State the blood parasite species.
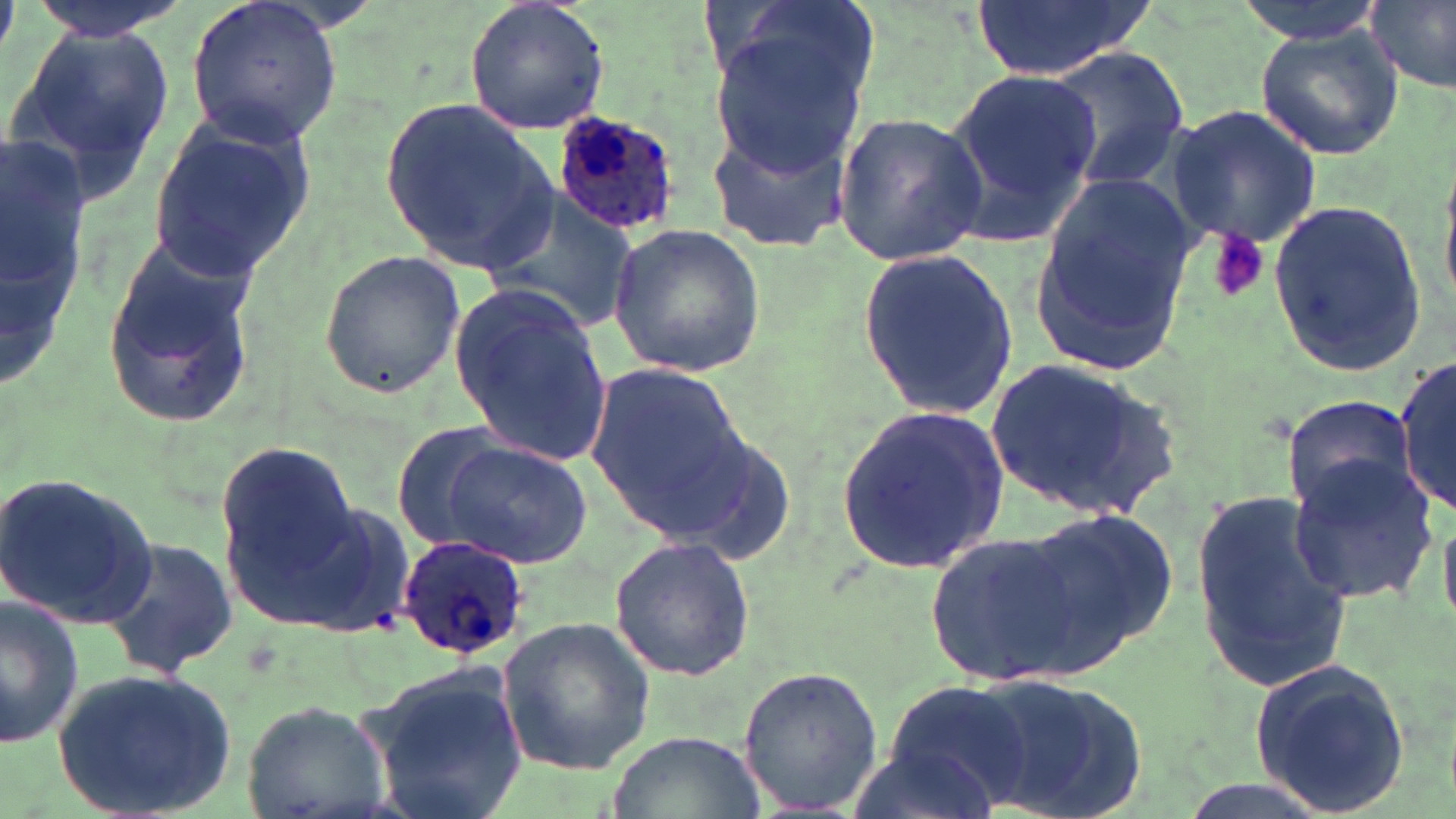
Plasmodium ovale.

image size = 1456×819 pixels
stain = May-Grünwald-Giemsa
platelet locations = approximate bounding boxes as [x1, y1, x2, y2] in pixels: [1207, 232, 1270, 303]
field of view = one of a larger specimen
preparation = thin blood film
uninfected red blood cell locations = approximate bounding boxes as [x1, y1, x2, y2] in pixels: [29, 0, 192, 40], [468, 0, 609, 137], [971, 0, 1154, 83], [1230, 0, 1391, 42], [1365, 0, 1456, 95], [185, 1, 346, 147], [707, 10, 878, 178], [1253, 19, 1405, 161], [4, 23, 179, 200], [1049, 48, 1188, 190], [943, 65, 1101, 242], [381, 95, 562, 278], [1166, 103, 1321, 249], [832, 111, 989, 265], [148, 114, 312, 280], [707, 119, 850, 252], [3, 123, 92, 404], [481, 185, 641, 332], [1029, 186, 1195, 369], [1266, 197, 1428, 376], [607, 223, 767, 377], [98, 229, 263, 429], [858, 246, 1022, 419], [317, 249, 468, 400], [448, 287, 612, 471], [1394, 357, 1454, 515], [986, 358, 1182, 521], [586, 359, 747, 531], [1282, 395, 1421, 521], [835, 402, 1010, 578], [390, 428, 517, 550], [442, 438, 593, 569], [214, 444, 357, 582], [1286, 459, 1437, 605], [2, 470, 160, 626], [229, 485, 412, 639], [1190, 487, 1357, 695], [1005, 504, 1180, 678], [924, 529, 1087, 687], [609, 534, 756, 681], [101, 536, 236, 681], [0, 595, 84, 750], [497, 617, 655, 776], [1247, 656, 1412, 816], [358, 661, 529, 819], [736, 663, 884, 816], [56, 664, 237, 819], [967, 673, 1149, 819], [881, 679, 1032, 809], [242, 699, 393, 819], [604, 729, 769, 819], [844, 741, 1002, 819]
Plasmodium ovale-infected red blood cell locations = approximate bounding boxes as [x1, y1, x2, y2] in pixels: [551, 107, 685, 240], [397, 532, 530, 659]
modality = light microscopy
magnification = 1000x